Assess this cell for malaria.
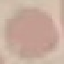
It is uninfected.

Summary:
  - Preparation: thin smear
  - Capture: smartphone through the microscope eyepiece
  - Image type: automatically extracted cell patch, resized to 64 × 64 pixels
  - Stain: Giemsa